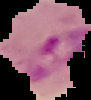

From a thin blood film. Result: Plasmodium parasites identified. Image is 91×100 pixels. The area outside the segmented cell region is set to black.